Name the blood parasite species.
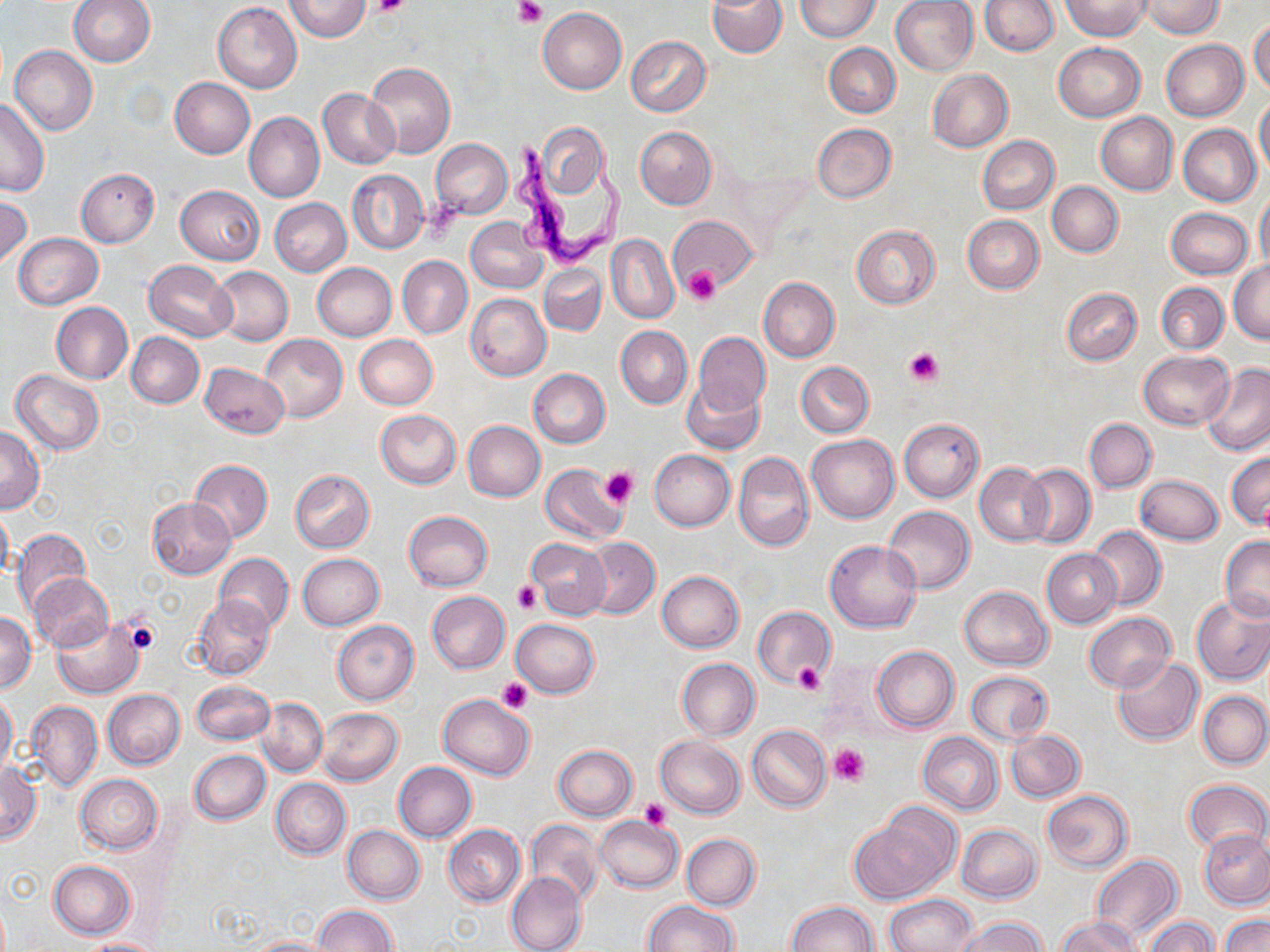
Trypanosoma brucei.

{
  "preparation": "thin blood smear",
  "stain": "May-Grünwald-Giemsa",
  "trypanosoma_brucei_locations": "approximate bounding boxes as [x1, y1, x2, y2] in pixels: [507, 133, 627, 271]",
  "uninfected_red_blood_cell_locations": "approximate bounding boxes as [x1, y1, x2, y2] in pixels: [36, 0, 146, 97], [69, 0, 155, 66], [284, 0, 370, 42], [707, 0, 787, 57], [796, 0, 881, 42], [890, 0, 979, 76], [979, 0, 1060, 55], [1062, 0, 1149, 39], [1142, 0, 1225, 38], [213, 2, 302, 92], [537, 7, 627, 95], [1249, 20, 1270, 93], [626, 36, 711, 117], [1161, 40, 1248, 121], [824, 43, 901, 118], [1053, 43, 1144, 121], [10, 46, 98, 135], [365, 62, 455, 158], [927, 69, 1013, 151], [168, 78, 255, 159], [318, 88, 399, 168], [1254, 97, 1270, 178], [0, 98, 50, 197], [244, 111, 324, 202], [1096, 113, 1178, 194], [533, 121, 610, 203], [812, 123, 895, 203], [1178, 124, 1260, 206], [635, 126, 717, 209], [978, 135, 1059, 214], [431, 139, 512, 219], [76, 168, 159, 247], [347, 170, 428, 253], [1047, 181, 1123, 256], [176, 185, 264, 264], [1255, 191, 1270, 272], [0, 196, 31, 268], [269, 198, 351, 276], [1167, 208, 1253, 279], [669, 215, 756, 292], [962, 215, 1045, 293], [466, 216, 547, 294], [851, 224, 941, 309], [13, 233, 103, 309], [607, 234, 679, 323], [397, 256, 473, 338], [144, 259, 237, 341], [1229, 260, 1270, 343], [311, 263, 397, 341], [539, 263, 607, 336], [209, 265, 293, 346], [759, 277, 840, 362], [1157, 282, 1228, 353], [1061, 287, 1142, 366], [466, 293, 551, 381], [51, 302, 132, 384], [616, 325, 692, 408], [126, 332, 204, 408], [694, 332, 771, 414], [261, 333, 348, 422], [354, 335, 438, 410], [1138, 350, 1233, 431], [797, 361, 874, 437], [199, 362, 289, 439], [1201, 363, 1270, 455], [11, 369, 105, 455], [528, 369, 610, 448], [681, 378, 765, 454], [375, 409, 460, 489], [899, 418, 984, 501], [1085, 418, 1157, 493], [463, 420, 545, 502], [0, 425, 44, 513], [806, 434, 900, 524], [649, 448, 735, 531], [733, 450, 814, 552], [1226, 451, 1270, 530], [188, 460, 273, 543], [975, 463, 1052, 546], [539, 464, 628, 544], [1019, 464, 1095, 547], [290, 469, 374, 552], [1135, 474, 1223, 546], [147, 497, 236, 579], [0, 505, 13, 582], [884, 505, 975, 594], [404, 510, 493, 592], [1088, 526, 1165, 609], [12, 529, 91, 613], [1219, 535, 1270, 621], [583, 537, 660, 619], [527, 538, 611, 620], [825, 540, 922, 633], [1042, 549, 1120, 628], [214, 553, 293, 631], [297, 553, 385, 629], [657, 571, 745, 652], [30, 573, 113, 652], [958, 585, 1053, 670], [426, 590, 510, 673], [193, 595, 275, 681], [1192, 596, 1270, 685], [753, 607, 834, 686], [0, 612, 37, 693], [1083, 612, 1175, 691], [51, 619, 145, 698], [511, 619, 600, 698], [332, 620, 419, 704], [872, 646, 958, 732], [1112, 656, 1203, 745], [676, 658, 760, 740], [966, 670, 1053, 745], [191, 678, 273, 745], [103, 689, 185, 769], [1198, 691, 1270, 769], [0, 692, 17, 772], [438, 692, 535, 780], [256, 697, 327, 775], [27, 701, 102, 790], [317, 707, 402, 786], [747, 724, 831, 812], [1005, 729, 1085, 803], [918, 732, 1003, 814], [655, 735, 745, 818], [552, 745, 637, 820], [189, 750, 271, 824], [392, 762, 477, 842], [1, 763, 40, 844], [75, 774, 164, 853], [271, 778, 351, 859], [1182, 779, 1269, 856], [1042, 790, 1133, 872], [851, 810, 956, 903], [595, 816, 683, 892], [525, 820, 604, 905], [443, 824, 525, 906], [956, 824, 1042, 902], [343, 825, 425, 903], [1200, 828, 1270, 908], [681, 833, 760, 910], [1090, 855, 1182, 945], [48, 861, 135, 939], [506, 871, 587, 952], [885, 894, 978, 952], [645, 900, 738, 952], [788, 901, 878, 952], [312, 905, 396, 951], [1220, 913, 1270, 952], [1056, 916, 1141, 952], [1143, 916, 1218, 952], [958, 917, 1046, 952], [248, 936, 343, 951], [77, 937, 165, 951]",
  "image_size": "1270×952 pixels",
  "platelet_locations": "approximate bounding boxes as [x1, y1, x2, y2] in pixels: [372, 0, 409, 19], [514, 0, 546, 26], [426, 199, 465, 242], [685, 268, 719, 306], [905, 347, 942, 389], [600, 466, 640, 509], [513, 581, 541, 614], [120, 613, 161, 655], [793, 663, 825, 694], [499, 678, 532, 714], [828, 743, 871, 785], [639, 799, 670, 829]",
  "magnification": "1000x",
  "modality": "optical microscopy",
  "field_of_view": "single"
}